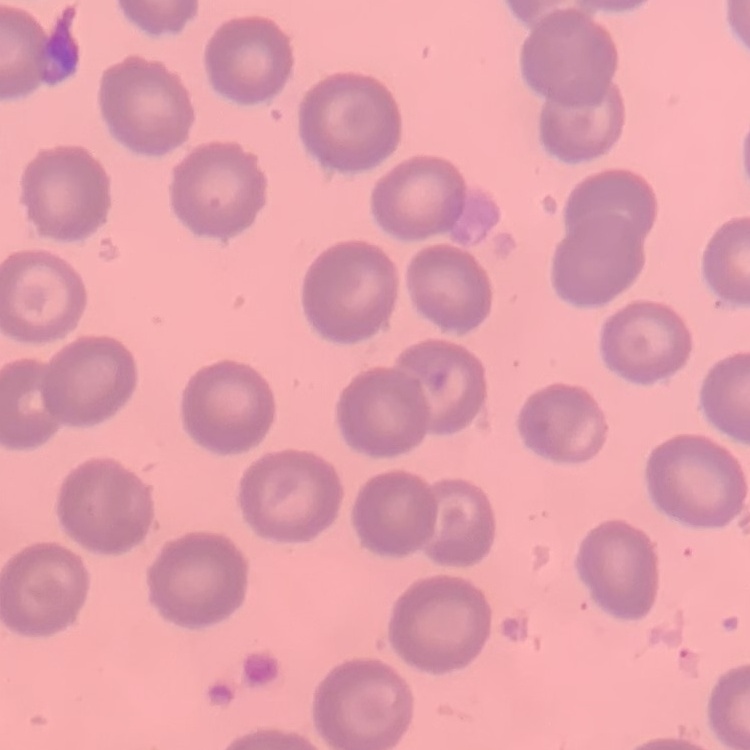

erythrocyte_morphology: no rouleaux formation
stain: Field's or Giemsa
image_type: square crop of a larger photomicrograph
preparation: thin blood smear